State which cell type is depicted.
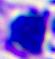
This is a leukocyte.

modality: micrograph
magnification: 400x